Give the position of every Plasmodium parasite visible.
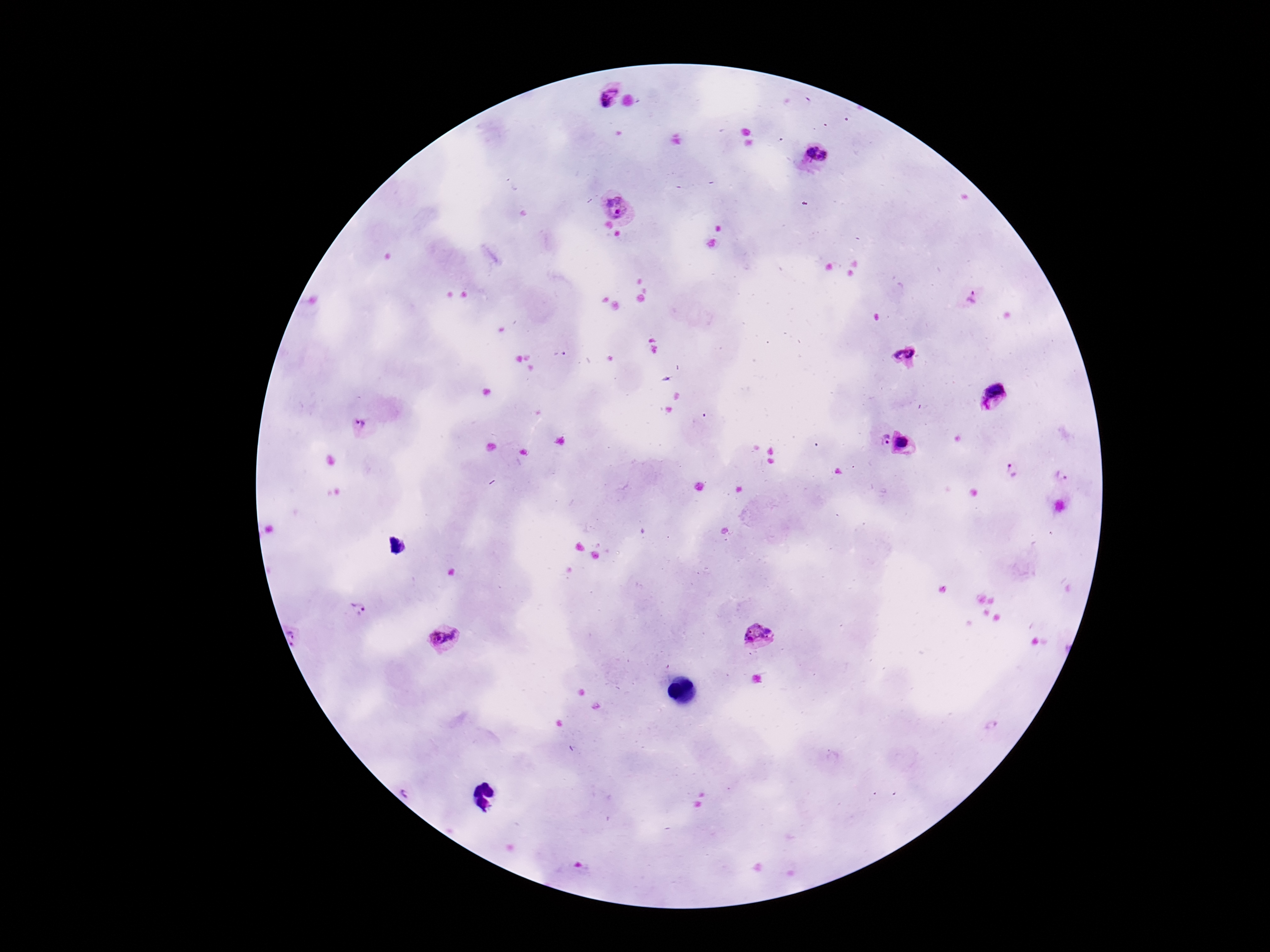

Approximate centers as (x, y) in pixels.
Plasmodium parasites: (605, 92), (815, 159), (620, 201), (973, 297), (909, 354), (995, 395), (365, 430), (876, 438), (904, 444), (1014, 472), (1061, 475), (358, 607), (299, 634), (444, 636), (756, 636).

Summary:
  - Capture: smartphone camera through the microscope eyepiece
  - Preparation: thick blood film
  - Stain: Giemsa
  - Magnification: 100x
  - Image size: 1270×952 pixels
  - Field of view: single
  - Patient malaria status: infected